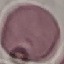 Result: no malaria parasites seen. Thin blood smear. Photographed with a smartphone camera at the microscope eyepiece. Cell patch, automatically extracted from a larger field of view and resized to 64 × 64 pixels. Giemsa stain.